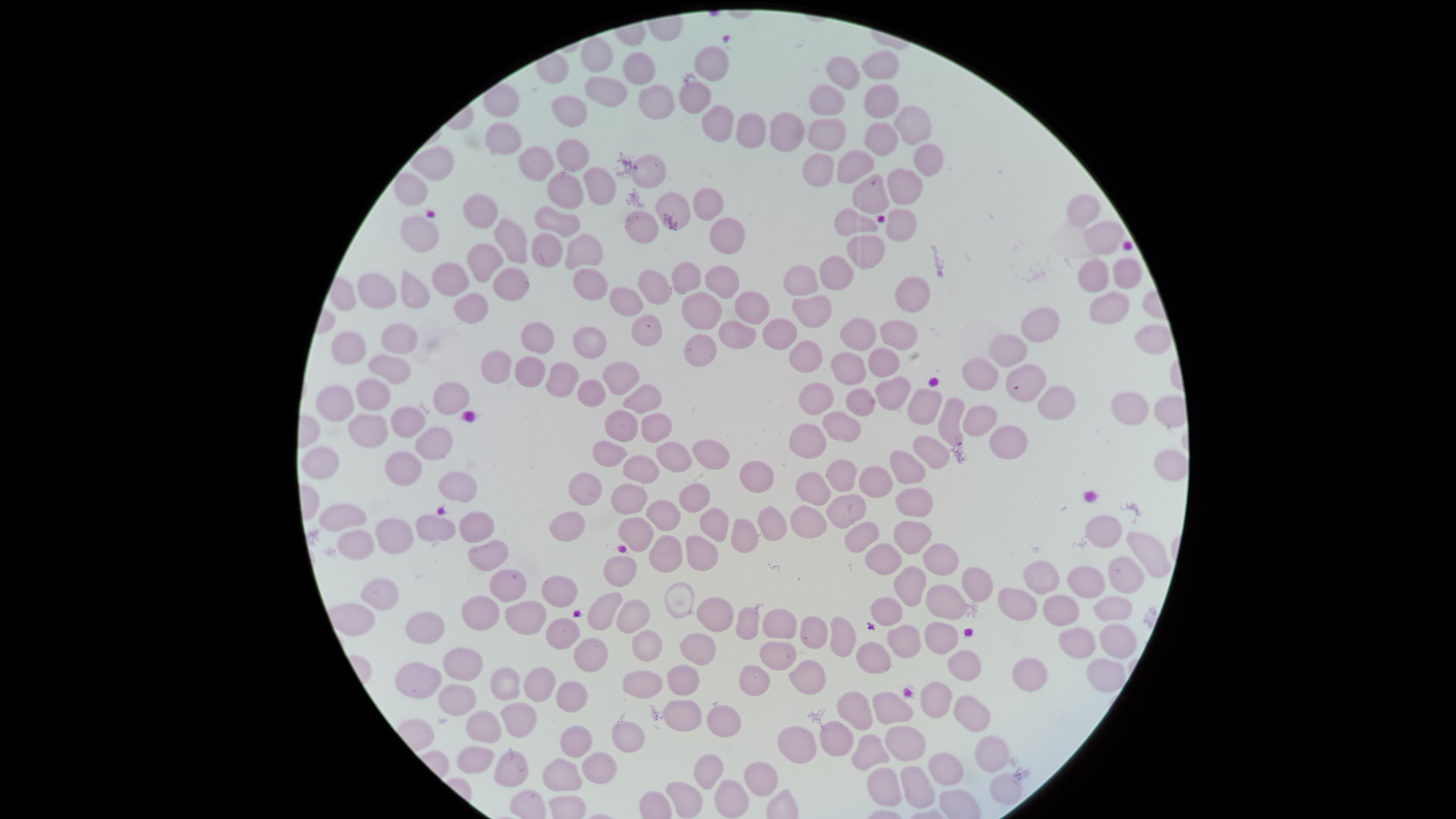
Approximate marker points, in pixels from the top-left corner.
Summary:
  - Uninfected red blood cells: (x=589, y=46), (x=710, y=57), (x=879, y=62), (x=635, y=69), (x=842, y=73), (x=599, y=83), (x=884, y=97), (x=694, y=99), (x=820, y=100), (x=649, y=102), (x=578, y=115), (x=917, y=116), (x=726, y=122), (x=750, y=127), (x=827, y=134), (x=881, y=134), (x=778, y=138), (x=504, y=140), (x=570, y=153), (x=933, y=157), (x=535, y=160), (x=439, y=163), (x=820, y=170), (x=854, y=170), (x=652, y=174), (x=597, y=185), (x=562, y=187), (x=406, y=189), (x=904, y=189), (x=866, y=198), (x=679, y=203), (x=709, y=205), (x=480, y=206), (x=1086, y=209), (x=561, y=215), (x=897, y=223), (x=853, y=225), (x=640, y=230), (x=420, y=231), (x=728, y=232), (x=1098, y=237), (x=515, y=244), (x=868, y=247), (x=580, y=248), (x=545, y=249), (x=482, y=263), (x=1093, y=272), (x=1122, y=272), (x=724, y=276), (x=584, y=277), (x=686, y=278), (x=830, y=278), (x=445, y=282), (x=511, y=282), (x=804, y=283), (x=654, y=284), (x=410, y=290), (x=379, y=292), (x=910, y=292), (x=626, y=302), (x=749, y=303), (x=1108, y=303), (x=469, y=308), (x=702, y=308), (x=814, y=309), (x=1046, y=324), (x=647, y=325), (x=740, y=326), (x=899, y=330), (x=776, y=331), (x=857, y=331), (x=588, y=333), (x=398, y=337), (x=540, y=337), (x=350, y=342), (x=697, y=349), (x=1018, y=351), (x=884, y=359), (x=499, y=360), (x=813, y=361), (x=533, y=366), (x=849, y=366), (x=383, y=367), (x=618, y=373), (x=984, y=378), (x=563, y=380), (x=1026, y=380), (x=891, y=386), (x=589, y=389), (x=376, y=391), (x=449, y=394), (x=821, y=395), (x=863, y=395), (x=639, y=400), (x=338, y=401), (x=922, y=402), (x=1123, y=404), (x=1060, y=406), (x=983, y=418), (x=402, y=421), (x=949, y=421), (x=366, y=424), (x=845, y=425), (x=626, y=426), (x=648, y=430), (x=812, y=435), (x=427, y=442), (x=604, y=444), (x=1016, y=446), (x=707, y=452), (x=934, y=452), (x=666, y=455), (x=329, y=463), (x=637, y=463), (x=907, y=466), (x=1164, y=468), (x=843, y=470), (x=404, y=474), (x=872, y=474), (x=758, y=475), (x=815, y=481), (x=458, y=489), (x=586, y=489), (x=691, y=494), (x=634, y=496), (x=915, y=497), (x=852, y=505), (x=352, y=511), (x=660, y=513), (x=566, y=518), (x=718, y=523), (x=769, y=523), (x=805, y=524), (x=1102, y=526), (x=478, y=527), (x=434, y=528), (x=639, y=532), (x=741, y=532), (x=391, y=534), (x=907, y=534), (x=860, y=535), (x=1136, y=544), (x=357, y=545), (x=703, y=550), (x=670, y=551), (x=485, y=553), (x=876, y=557), (x=938, y=557), (x=620, y=571), (x=1045, y=575), (x=1114, y=577), (x=1083, y=582), (x=502, y=583), (x=973, y=583), (x=907, y=587), (x=378, y=591), (x=560, y=594), (x=1019, y=597), (x=678, y=599), (x=607, y=603), (x=941, y=607), (x=641, y=608), (x=1062, y=608), (x=355, y=612), (x=710, y=612), (x=1111, y=612), (x=896, y=614), (x=484, y=615), (x=530, y=618), (x=744, y=624), (x=779, y=627), (x=426, y=630), (x=815, y=633), (x=558, y=634), (x=837, y=635), (x=937, y=638), (x=648, y=642), (x=902, y=642), (x=1071, y=642), (x=1111, y=643), (x=695, y=644), (x=592, y=648), (x=779, y=658), (x=463, y=660), (x=870, y=660), (x=965, y=665), (x=1027, y=671), (x=1095, y=672), (x=677, y=675), (x=417, y=677), (x=804, y=677), (x=641, y=678), (x=540, y=680), (x=755, y=684), (x=938, y=695), (x=569, y=697), (x=450, y=699), (x=886, y=707), (x=965, y=709), (x=680, y=710), (x=523, y=715), (x=859, y=715), (x=480, y=720), (x=732, y=720), (x=628, y=736), (x=790, y=736), (x=906, y=737), (x=829, y=741), (x=573, y=744), (x=869, y=748), (x=992, y=748), (x=473, y=753), (x=601, y=761), (x=947, y=763), (x=508, y=767), (x=764, y=770), (x=558, y=771), (x=711, y=773), (x=885, y=785), (x=924, y=785), (x=1003, y=788), (x=684, y=797), (x=730, y=797)
  - Presence: no malaria parasites detected
  - Field of view: single
  - Visible region: circular
  - Image size: 1456×819 pixels
  - Capture: smartphone photograph through the microscope eyepiece
  - Preparation: thin blood film
  - Stain: Giemsa